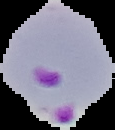

Summary:
  - Preparation: thin blood smear
  - Image type: segmented cell region with the area outside set to black
  - Image size: 115×130 pixels
  - Malaria status: parasitized